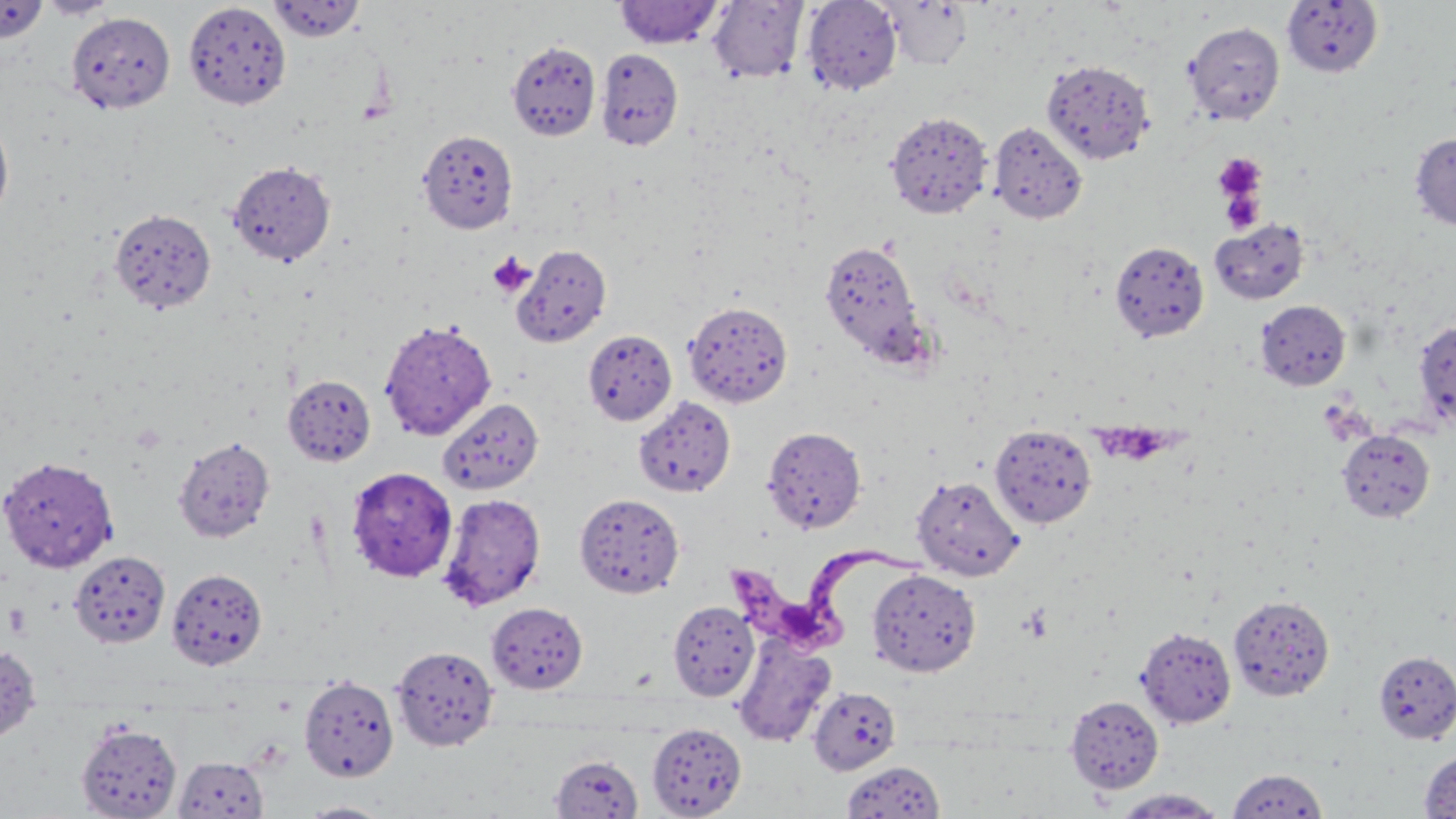
slide-level diagnosis = Trypanosoma brucei
platelet locations = approximate bounding boxes as named x1/y1/x2/y2 corners in pixels: (x1=1213, y1=152, x2=1267, y2=203), (x1=1218, y1=185, x2=1264, y2=234), (x1=487, y1=252, x2=536, y2=298), (x1=1102, y1=420, x2=1182, y2=466), (x1=1020, y1=604, x2=1053, y2=643)
magnification = 1000x
image size = 1456×819 pixels
preparation = thin blood film
Trypanosoma brucei locations = approximate bounding boxes as named x1/y1/x2/y2 corners in pixels: (x1=725, y1=532, x2=932, y2=654)
stain = May-Grünwald-Giemsa
field of view = single
modality = light microscopy
uninfected red blood cell locations = approximate bounding boxes as named x1/y1/x2/y2 corners in pixels: (x1=36, y1=0, x2=120, y2=19), (x1=802, y1=0, x2=902, y2=96), (x1=0, y1=1, x2=50, y2=44), (x1=183, y1=1, x2=292, y2=110), (x1=267, y1=1, x2=365, y2=42), (x1=614, y1=1, x2=724, y2=48), (x1=707, y1=1, x2=808, y2=83), (x1=881, y1=1, x2=973, y2=71), (x1=1281, y1=1, x2=1384, y2=77), (x1=66, y1=11, x2=176, y2=113), (x1=1183, y1=21, x2=1285, y2=125), (x1=506, y1=40, x2=600, y2=141), (x1=596, y1=48, x2=684, y2=150), (x1=1041, y1=58, x2=1154, y2=165), (x1=885, y1=111, x2=992, y2=219), (x1=0, y1=114, x2=15, y2=227), (x1=989, y1=121, x2=1088, y2=224), (x1=417, y1=129, x2=518, y2=234), (x1=1410, y1=132, x2=1456, y2=231), (x1=227, y1=160, x2=336, y2=266), (x1=110, y1=208, x2=217, y2=314), (x1=1209, y1=218, x2=1310, y2=305), (x1=819, y1=238, x2=928, y2=368), (x1=1110, y1=240, x2=1210, y2=342), (x1=513, y1=244, x2=612, y2=347), (x1=683, y1=300, x2=793, y2=408), (x1=1256, y1=300, x2=1351, y2=390), (x1=379, y1=319, x2=496, y2=440), (x1=1413, y1=320, x2=1456, y2=428), (x1=582, y1=328, x2=677, y2=424), (x1=283, y1=375, x2=376, y2=466), (x1=633, y1=396, x2=736, y2=498), (x1=438, y1=398, x2=544, y2=495), (x1=990, y1=423, x2=1097, y2=528), (x1=762, y1=426, x2=867, y2=533), (x1=1338, y1=430, x2=1435, y2=522), (x1=173, y1=435, x2=275, y2=543), (x1=0, y1=456, x2=117, y2=572), (x1=346, y1=466, x2=458, y2=582), (x1=912, y1=475, x2=1024, y2=581), (x1=574, y1=492, x2=684, y2=598), (x1=437, y1=493, x2=546, y2=611), (x1=69, y1=550, x2=170, y2=649), (x1=167, y1=568, x2=268, y2=670), (x1=867, y1=568, x2=981, y2=677), (x1=1228, y1=594, x2=1335, y2=701), (x1=667, y1=600, x2=759, y2=701), (x1=486, y1=602, x2=589, y2=693), (x1=1136, y1=626, x2=1236, y2=728), (x1=733, y1=633, x2=836, y2=747), (x1=0, y1=644, x2=41, y2=745), (x1=391, y1=645, x2=499, y2=751), (x1=1373, y1=650, x2=1456, y2=743), (x1=299, y1=675, x2=399, y2=781), (x1=808, y1=686, x2=901, y2=775), (x1=1065, y1=695, x2=1164, y2=793), (x1=76, y1=721, x2=182, y2=818), (x1=647, y1=723, x2=746, y2=818), (x1=1420, y1=749, x2=1456, y2=817), (x1=550, y1=755, x2=643, y2=818), (x1=173, y1=756, x2=268, y2=818), (x1=841, y1=760, x2=946, y2=818), (x1=1226, y1=768, x2=1329, y2=817), (x1=1110, y1=789, x2=1228, y2=818), (x1=296, y1=801, x2=394, y2=818)